Outline each blood parasite and name the species.
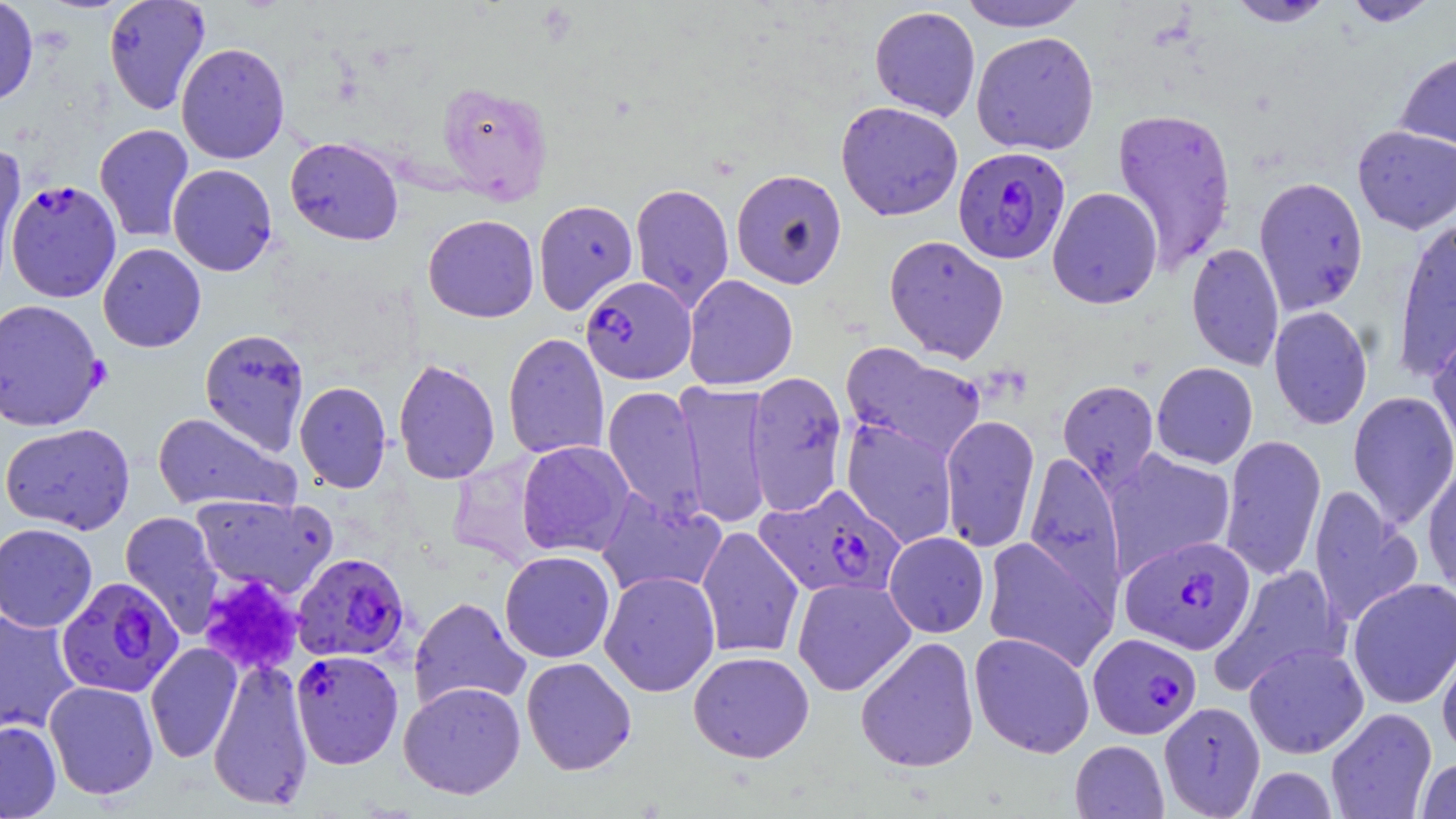

Approximate bounding boxes as (x1, y1, x2, y2) in pixels.
Plasmodium falciparum-infected red blood cells: (952, 146, 1071, 264), (5, 179, 122, 303), (579, 276, 695, 385), (754, 483, 906, 601), (1120, 535, 1256, 655), (291, 552, 412, 663), (56, 576, 183, 698), (1087, 632, 1202, 739), (290, 649, 404, 769).
No Plasmodium ovale, Plasmodium malariae, Plasmodium vivax, Babesia divergens, or Trypanosoma brucei observed.

slide_level_diagnosis: Plasmodium falciparum
preparation: thin blood film
modality: optical microscopy
magnification: 1000x
image_size: 1456×819 pixels
field_of_view: single
stain: May-Grünwald-Giemsa
uninfected_red_blood_cell_locations: 'approximate bounding boxes as (x1, y1, x2, y2) in pixels: (0, 0, 39, 107), (103, 0, 211, 115), (957, 0, 1088, 32), (1342, 0, 1441, 26), (1226, 1, 1336, 27), (869, 5, 981, 122), (970, 31, 1100, 156), (175, 42, 290, 164), (1395, 48, 1456, 155), (436, 81, 553, 205), (835, 101, 964, 221), (1111, 106, 1237, 271), (95, 123, 194, 243), (1353, 125, 1456, 234), (285, 137, 404, 245), (0, 143, 28, 295), (167, 163, 278, 276), (731, 169, 847, 288), (1254, 175, 1369, 315), (630, 183, 734, 312), (1047, 187, 1163, 309), (533, 199, 638, 315), (423, 214, 539, 323), (1391, 217, 1455, 380), (883, 235, 1009, 363), (98, 243, 206, 352), (1186, 243, 1284, 371), (683, 275, 798, 390), (0, 298, 107, 432), (1268, 305, 1373, 430), (199, 328, 309, 454), (1427, 328, 1456, 462), (502, 332, 610, 460), (840, 342, 988, 464), (393, 358, 500, 485), (1151, 362, 1258, 469), (745, 371, 849, 517), (1057, 379, 1159, 490), (295, 381, 392, 493), (674, 381, 774, 529), (602, 384, 708, 523), (1347, 390, 1456, 530), (153, 411, 298, 514), (939, 414, 1040, 554), (841, 417, 959, 549), (1, 422, 135, 535), (1219, 434, 1326, 581), (516, 440, 635, 557), (1103, 449, 1236, 577), (1023, 451, 1126, 608), (1422, 458, 1456, 596), (1308, 486, 1422, 630), (596, 489, 727, 599), (191, 493, 335, 598), (120, 510, 226, 638), (0, 523, 98, 632), (696, 525, 805, 659), (883, 532, 989, 637), (982, 536, 1116, 672), (500, 550, 615, 663), (1211, 564, 1348, 695), (599, 570, 721, 697), (792, 577, 916, 696), (1347, 577, 1456, 709), (409, 596, 531, 713), (0, 609, 81, 738), (969, 632, 1095, 758), (855, 635, 980, 773), (1437, 635, 1456, 762), (145, 642, 243, 764), (1243, 643, 1369, 759), (688, 651, 815, 762), (207, 657, 314, 812), (521, 657, 636, 775), (43, 681, 159, 800), (398, 681, 526, 799), (1159, 701, 1265, 817), (1325, 707, 1437, 819), (0, 720, 61, 819), (1070, 740, 1168, 818), (1415, 758, 1456, 818), (1244, 766, 1338, 818)'
platelet_locations: 'approximate bounding boxes as (x1, y1, x2, y2) in pixels: (199, 576, 305, 677)'